Classify this cell by malaria status.
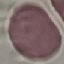
It is uninfected.

capture = smartphone through the microscope eyepiece
image type = automatically extracted cell patch, resized to 64 × 64 pixels
stain = Giemsa
preparation = thin blood film